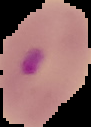
result = malaria parasites identified
preparation = thin blood film
image size = 91×127 pixels
image type = segmented cell region on a black background